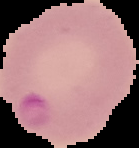
Summary:
  - Image type: segmented cell region on a black background
  - Malaria status: parasitized
  - Image size: 139×148 pixels
  - Preparation: thin blood film